State which parasite is depicted.
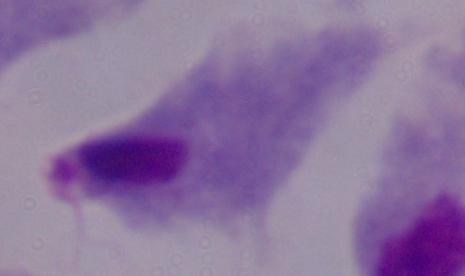

A trichomonad.

Summary:
  - Magnification: 1000x
  - Modality: photomicrograph